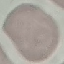

Summary:
  - Result: no malaria parasites seen
  - Preparation: thin blood smear
  - Image type: cell patch, automatically extracted from a larger field of view and resized to 64 × 64 pixels
  - Capture: smartphone camera at the microscope eyepiece
  - Stain: Giemsa